Report the malaria status of this cell.
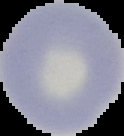
It is uninfected.

Image is 124×136 pixels. Cell region segmented out of the field of view; the surrounding area is masked to black. From a thin blood film.